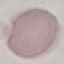

result: no malaria parasites seen
image_type: cell patch, automatically extracted from a larger field of view and resized to 64 × 64 pixels
stain: Giemsa
preparation: thin smear
capture: smartphone through the microscope eyepiece